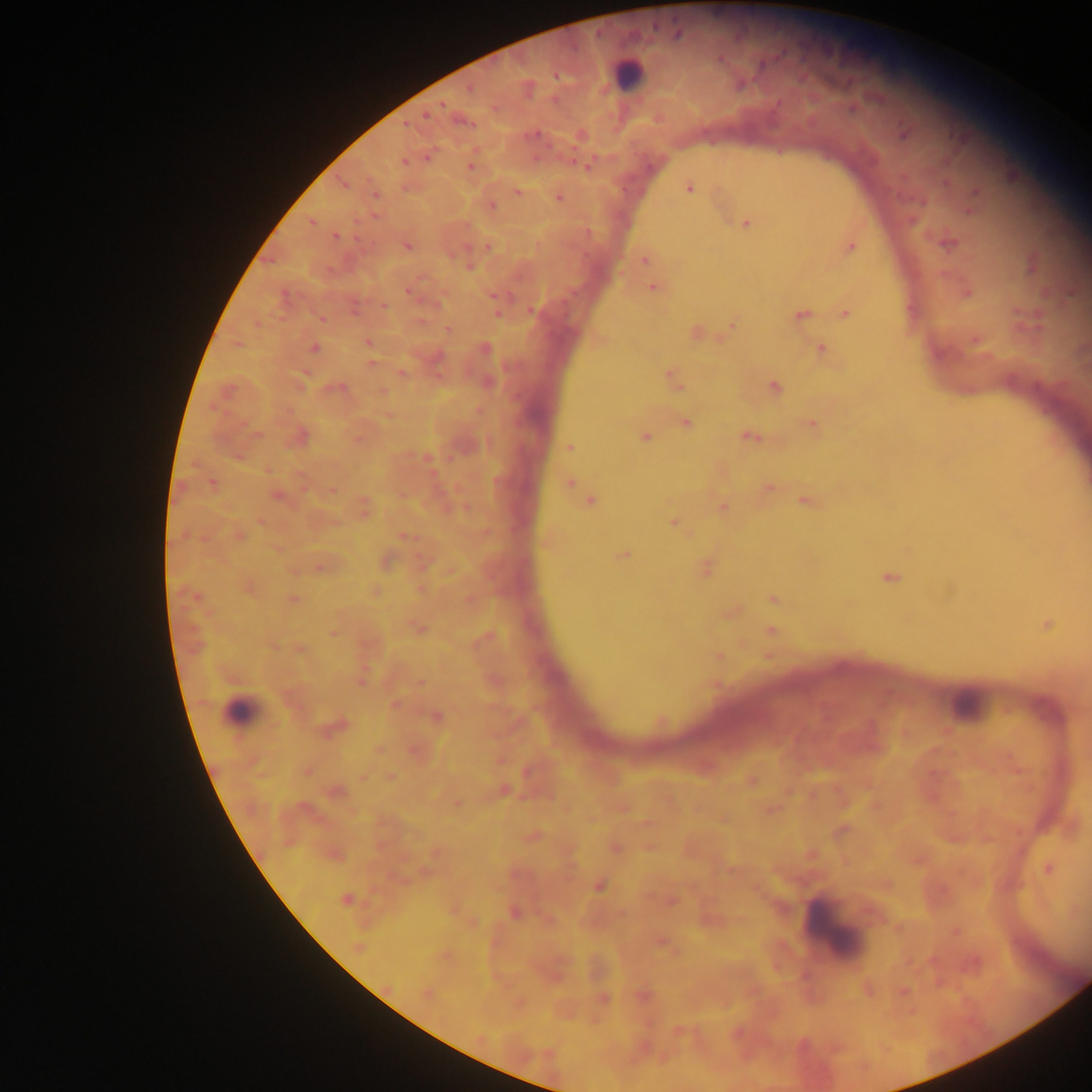
Approximate centers as {x, y} in pixels. Plasmodium parasite locations: {678, 34}, {469, 89}, {442, 105}, {426, 113}, {903, 133}, {580, 135}, {428, 155}, {404, 161}, {470, 166}, {586, 166}, {342, 183}, {688, 187}, {975, 191}, {517, 192}, {374, 194}, {558, 197}, {491, 205}, {969, 209}, {311, 221}, {746, 222}, {336, 236}, {947, 242}, {407, 245}, {488, 246}, {850, 246}, {643, 260}, {1032, 264}, {469, 266}, {653, 287}, {407, 290}, {966, 292}, {494, 295}, {284, 296}, {354, 305}, {383, 305}, {529, 311}, {497, 313}, {845, 313}, {800, 314}, {321, 318}, {731, 324}, {448, 330}, {695, 332}, {975, 339}, {368, 342}, {314, 348}, {484, 349}, {820, 349}, {370, 363}, {402, 373}, {672, 377}, {774, 386}, {335, 387}, {382, 392}, {389, 415}, {685, 423}, {811, 424}, {299, 436}, {644, 436}, {750, 436}, {357, 438}, {569, 447}, {569, 482}, {212, 483}, {766, 488}, {332, 489}, {276, 495}, {591, 501}, {805, 501}, {723, 507}, {363, 508}, {674, 522}, {239, 535}, {404, 536}, {545, 542}, {624, 554}, {384, 561}, {423, 564}, {321, 566}, {706, 568}, {449, 571}, {889, 577}, {248, 587}, {421, 589}, {375, 590}, {773, 598}, {292, 599}, {469, 600}, {730, 612}, {1047, 624}, {418, 628}, {333, 631}, {770, 631}, {484, 638}, {299, 649}, {718, 656}, {361, 680}, {420, 681}, {394, 704}, {436, 716}, {333, 727}, {378, 750}, {415, 750}, {1018, 769}, {307, 770}, {363, 776}, {390, 777}, {751, 780}, {503, 790}, {335, 791}, {456, 803}, {770, 810}, {840, 830}, {531, 836}, {615, 847}, {435, 853}, {334, 854}, {1048, 868}, {598, 885}, {346, 899}, {671, 901}, {513, 912}, {472, 923}, {956, 931}, {661, 941}, {358, 946}, {444, 955}, {973, 964}, {868, 989}, {903, 991}, {426, 993}, {642, 995}, {602, 998}, {517, 1003}, {679, 1031}, {644, 1047}. Leukocyte locations: {628, 75}, {967, 704}, {239, 711}, {833, 928}. Image is 1092×1092 pixels. Photographed through a microscope with a mobile-phone camera. Collected in Ghana. One field of view. Thick blood film.